Point out Plasmodium parasites and leukocytes.
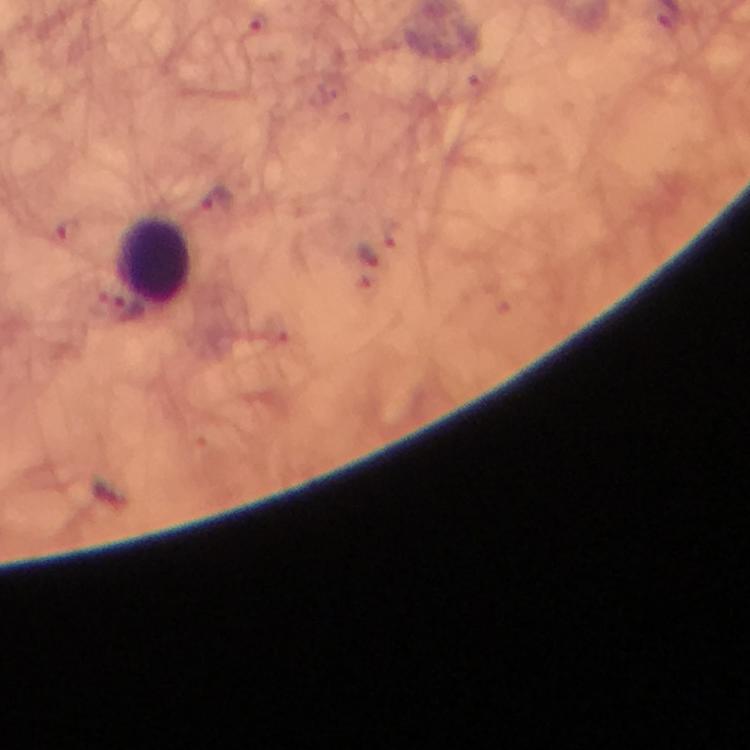
Approximate centers as {x, y} in pixels.
Plasmodium parasites: {259, 24}, {218, 204}, {66, 232}, {368, 255}.
Leukocytes: {155, 263}.

context: from a diagnostic examination for malaria
stain: Giemsa
image_size: 750×750 pixels
immersion_oil: used
magnification: 100x
capture: smartphone camera through the microscope
preparation: thick smear
cropped_from: a single field of view